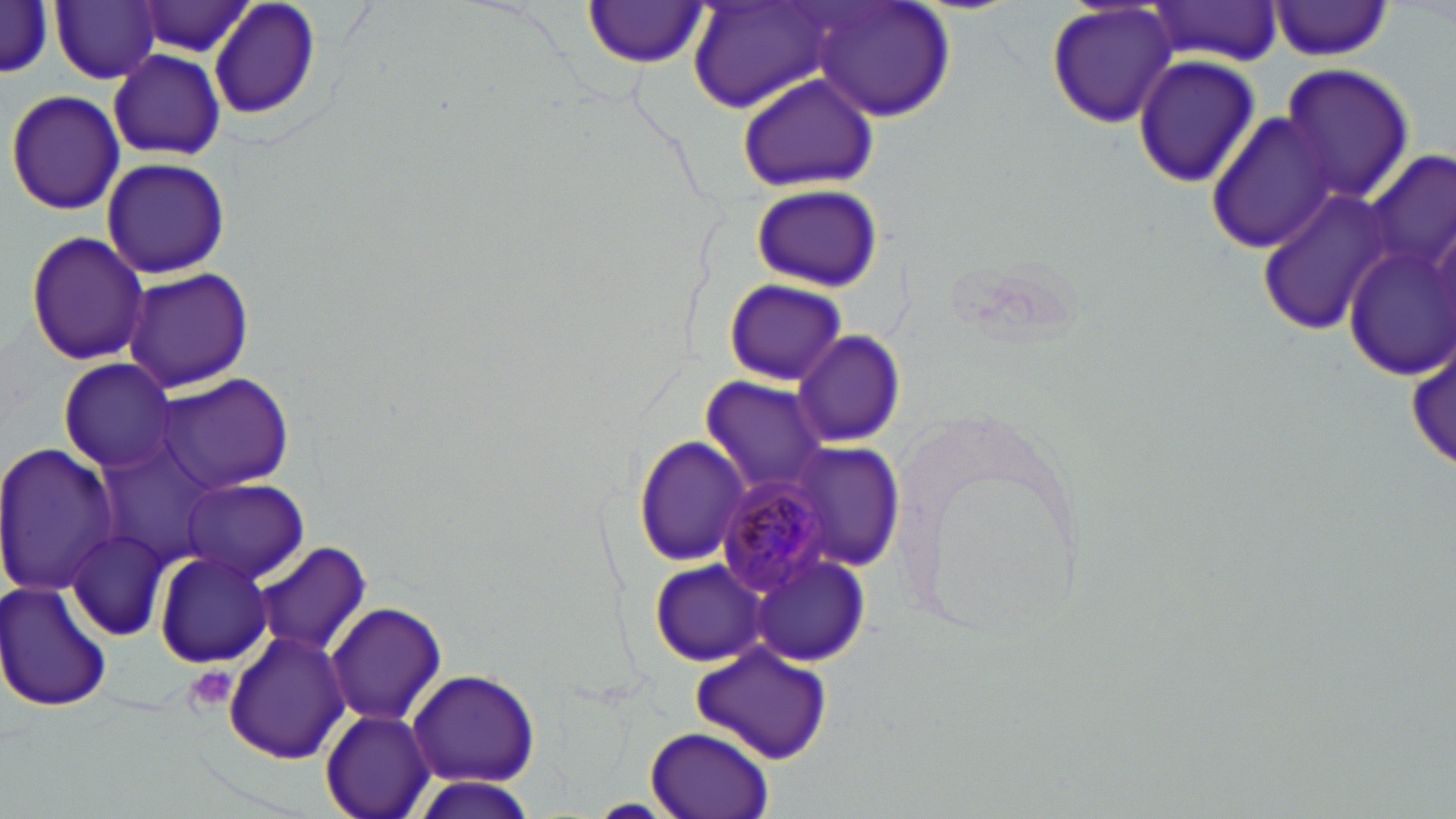
slide_level_diagnosis: Plasmodium malariae
field_of_view: single
modality: optical microscopy
uninfected_red_blood_cell_locations: 'approximate bounding boxes as [x1, y1, x2, y2] in pixels: [206, 0, 322, 123], [51, 1, 162, 84], [810, 1, 958, 122], [1045, 1, 1179, 130], [0, 2, 55, 81], [583, 2, 709, 69], [688, 2, 842, 115], [1269, 2, 1394, 60], [136, 3, 257, 57], [1147, 3, 1282, 65], [109, 50, 226, 160], [1130, 54, 1261, 188], [1278, 63, 1415, 203], [736, 72, 880, 192], [5, 90, 124, 215], [1206, 111, 1340, 254], [1364, 151, 1455, 284], [102, 156, 229, 280], [749, 184, 882, 291], [1259, 186, 1394, 334], [24, 231, 151, 365], [1339, 240, 1456, 379], [120, 268, 255, 393], [723, 279, 846, 383], [792, 330, 905, 447], [60, 359, 180, 474], [155, 373, 295, 494], [701, 376, 832, 493], [632, 432, 751, 568], [0, 441, 121, 596], [787, 446, 904, 573], [182, 478, 308, 583], [64, 532, 169, 640], [257, 543, 371, 658], [747, 549, 872, 665], [152, 550, 274, 668], [649, 560, 770, 666], [0, 581, 115, 714], [327, 603, 446, 725], [225, 630, 351, 763], [687, 643, 835, 765], [407, 667, 540, 786], [320, 709, 437, 819], [646, 725, 776, 819], [405, 776, 540, 819]'
plasmodium_malariae_infected_red_blood_cell_locations: 'approximate bounding boxes as [x1, y1, x2, y2] in pixels: [716, 472, 839, 600]'
preparation: thin blood film
magnification: 1000x
stain: May-Grünwald-Giemsa
platelet_locations: 'approximate bounding boxes as [x1, y1, x2, y2] in pixels: [183, 665, 238, 713]'
image_size: 1456×819 pixels